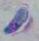
modality: photomicrograph
identification: Toxoplasma gondii
magnification: 1000x